Give the location of every parasitized red blood cell.
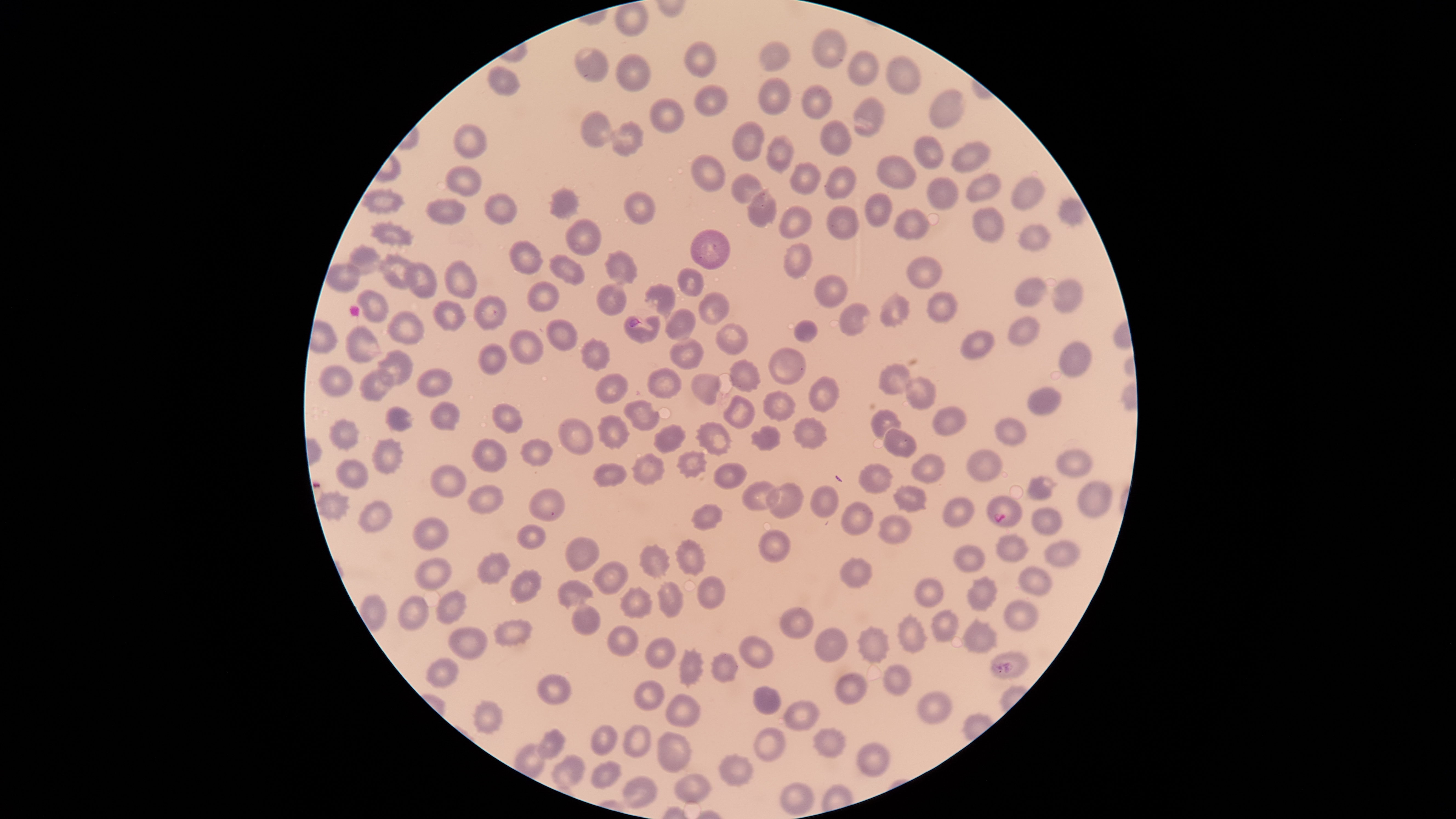

Approximate bounding boxes as (left, top, right, bottom) in pixels.
Parasitized red blood cells: (987, 496, 1023, 527).

Approximate bounding boxes as (left, top, right, bottom) in pixels. Uninfected red blood cells: (615, 1, 649, 36), (812, 28, 848, 68), (684, 41, 717, 77), (759, 41, 789, 73), (574, 44, 610, 83), (847, 50, 878, 86), (616, 53, 652, 92), (885, 56, 922, 96), (486, 65, 520, 97), (758, 78, 791, 114), (694, 83, 729, 117), (801, 84, 832, 120), (930, 90, 965, 129), (852, 95, 884, 136), (649, 98, 685, 133), (580, 110, 614, 147), (820, 119, 852, 156), (609, 121, 645, 157), (732, 121, 764, 161), (453, 123, 487, 158), (914, 134, 944, 169), (766, 135, 794, 174), (952, 141, 991, 174), (689, 153, 727, 192), (876, 154, 918, 190), (789, 162, 822, 195), (444, 165, 483, 199), (824, 167, 856, 201), (965, 171, 1001, 203), (730, 172, 764, 204), (1010, 176, 1046, 210), (927, 177, 958, 210), (547, 185, 582, 222), (362, 187, 405, 215), (746, 187, 778, 229), (624, 190, 656, 225), (484, 192, 517, 224), (865, 193, 892, 228), (424, 197, 465, 225), (1058, 197, 1084, 227), (776, 204, 813, 238), (826, 206, 861, 241), (972, 207, 1005, 242), (894, 208, 930, 240), (565, 217, 603, 256), (368, 220, 415, 249), (1017, 223, 1050, 252), (690, 228, 730, 270), (507, 240, 544, 276), (782, 242, 813, 278), (346, 243, 383, 276), (604, 249, 639, 286), (379, 252, 415, 290), (549, 255, 586, 286), (905, 255, 944, 289), (403, 260, 438, 299), (443, 260, 475, 299), (325, 263, 359, 293), (676, 268, 704, 296), (814, 276, 848, 309), (1015, 277, 1047, 308), (1051, 279, 1084, 315), (526, 281, 559, 312), (596, 281, 627, 316), (644, 283, 676, 320), (355, 288, 389, 322), (878, 290, 910, 328), (698, 291, 730, 325), (927, 291, 957, 325), (472, 295, 507, 331), (432, 300, 465, 331), (838, 302, 870, 336), (386, 309, 425, 345), (664, 309, 696, 341), (622, 314, 661, 345), (1007, 316, 1039, 347), (546, 319, 578, 351), (792, 319, 819, 343), (715, 323, 749, 356), (343, 325, 381, 366), (507, 328, 544, 365), (961, 329, 995, 358), (577, 336, 610, 371), (669, 337, 705, 371), (1058, 341, 1093, 378), (478, 343, 510, 375), (768, 347, 807, 385), (376, 349, 414, 387), (728, 359, 761, 393), (318, 363, 356, 399), (878, 363, 912, 395), (646, 365, 683, 399), (416, 367, 454, 398), (359, 370, 394, 401), (594, 372, 629, 404), (690, 374, 722, 406), (808, 376, 840, 412), (906, 376, 937, 409), (1027, 386, 1060, 416), (762, 389, 796, 422), (723, 395, 756, 429), (622, 398, 661, 431), (431, 401, 461, 432), (490, 403, 524, 436), (385, 406, 413, 431), (932, 406, 967, 437), (870, 409, 902, 438), (597, 414, 632, 451), (792, 416, 829, 451), (996, 416, 1026, 446), (328, 417, 362, 452), (557, 417, 594, 455), (695, 421, 733, 458), (652, 423, 687, 454), (750, 425, 781, 452), (882, 427, 916, 458), (370, 437, 405, 476), (471, 437, 508, 473), (519, 438, 553, 468), (1056, 449, 1093, 476), (675, 450, 709, 479), (965, 450, 1003, 483), (630, 453, 665, 487), (911, 453, 947, 484), (335, 458, 370, 490), (712, 462, 748, 490), (591, 463, 629, 488), (857, 463, 894, 494), (429, 464, 468, 498), (1027, 475, 1057, 501), (741, 479, 780, 512), (1076, 479, 1114, 518), (765, 481, 804, 519), (893, 484, 928, 513), (466, 485, 504, 516), (809, 485, 840, 519), (528, 488, 566, 522), (316, 489, 350, 522), (943, 496, 974, 530), (357, 500, 393, 533), (839, 502, 873, 537), (689, 503, 724, 532), (1031, 507, 1063, 535), (877, 513, 914, 545), (412, 516, 449, 552), (515, 524, 546, 550), (758, 529, 793, 562), (995, 532, 1030, 562), (565, 535, 600, 571), (674, 538, 707, 577), (1043, 539, 1081, 568), (638, 543, 672, 579), (952, 545, 986, 573), (476, 551, 511, 585), (415, 557, 451, 591), (839, 557, 874, 589), (593, 561, 628, 596), (1018, 566, 1053, 596), (509, 568, 543, 605), (697, 575, 726, 612), (965, 576, 998, 613), (914, 577, 944, 607), (557, 579, 594, 609), (657, 581, 685, 617), (619, 586, 653, 620), (434, 589, 468, 627), (398, 594, 429, 632), (570, 600, 602, 635), (1003, 600, 1039, 631), (779, 605, 813, 639), (931, 609, 958, 642), (895, 613, 929, 655), (961, 617, 999, 653), (493, 618, 534, 648), (606, 624, 640, 657), (857, 625, 891, 665), (448, 627, 488, 661), (814, 627, 849, 663), (738, 635, 774, 670), (645, 637, 676, 669), (677, 647, 705, 688), (990, 651, 1029, 679), (710, 652, 737, 684), (426, 657, 459, 687), (883, 663, 912, 696), (835, 672, 869, 706), (536, 673, 570, 706), (633, 679, 666, 711), (752, 685, 783, 715), (917, 690, 952, 725), (666, 694, 701, 728), (471, 699, 503, 736), (784, 700, 819, 731), (623, 723, 653, 758), (590, 724, 618, 757), (752, 725, 787, 762), (812, 726, 847, 760), (536, 727, 566, 760), (657, 730, 693, 774), (856, 741, 891, 778), (718, 753, 754, 788), (550, 754, 584, 791), (590, 760, 622, 790), (673, 773, 711, 805), (621, 776, 658, 810), (779, 782, 815, 817). Photographed with a smartphone camera through the microscope eyepiece. Species: Plasmodium falciparum. Single field of view. Giemsa-stained preparation. Circular visible region. Image is 1456×819 pixels. Thin blood film.